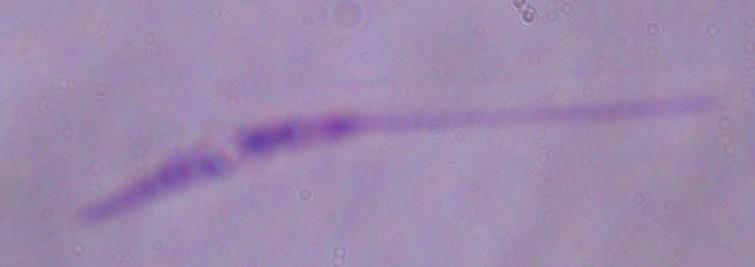

modality = photomicrograph
magnification = 1000x
identification = Leishmania